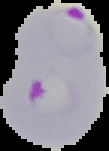

{
  "preparation": "thin blood smear",
  "malaria_status": "parasitized",
  "image_type": "segmented cell region on a black background",
  "image_size": "109×151 pixels"
}